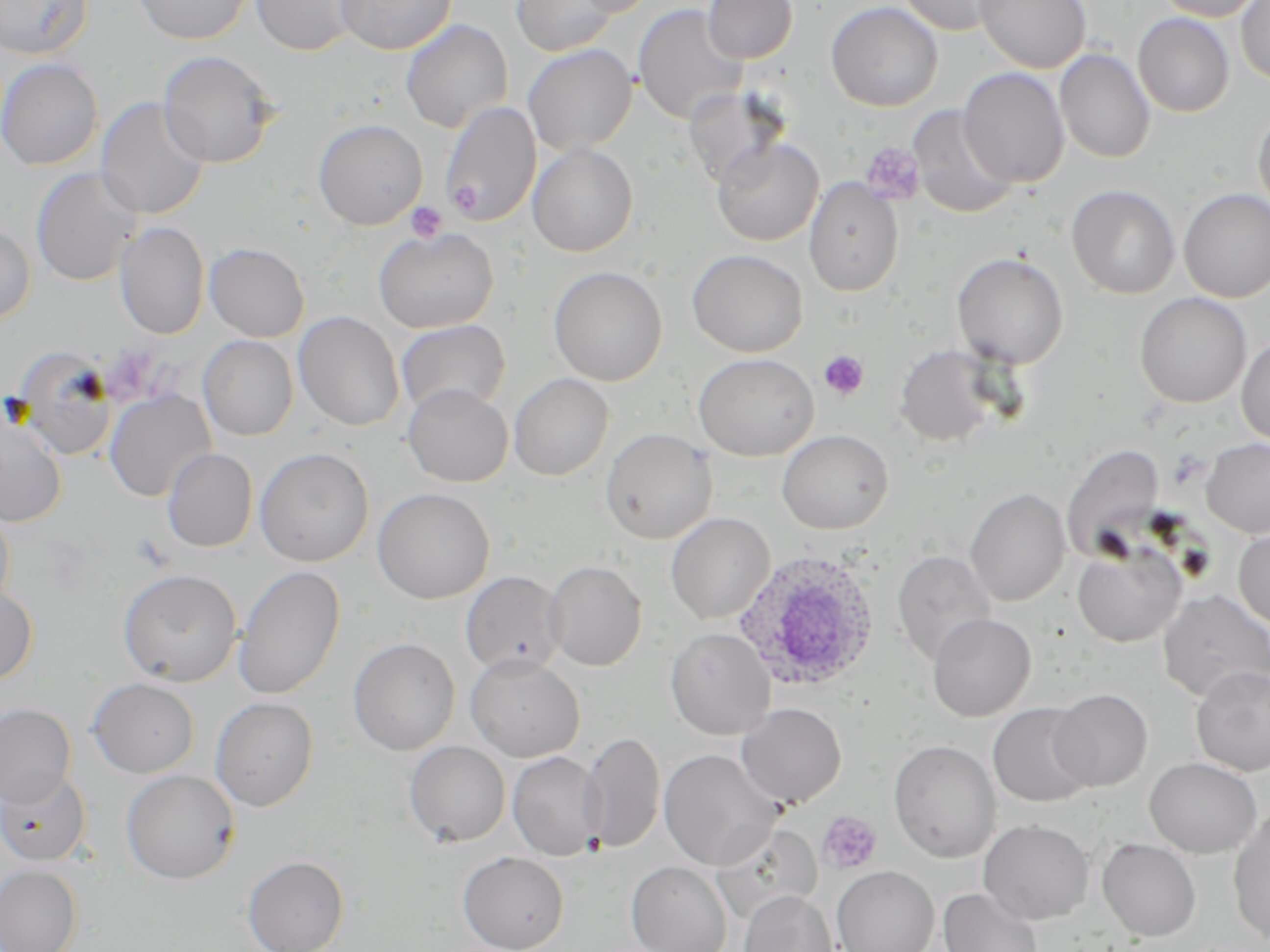
{
  "slide_level_diagnosis": "Plasmodium ovale",
  "preparation": "thin blood smear",
  "field_of_view": "single",
  "stain": "May-Grünwald-Giemsa",
  "magnification": "1000x",
  "platelet_locations": "approximate bounding boxes as named x1/y1/x2/y2 corners in pixels: (x1=859, y1=142, x2=926, y2=206), (x1=406, y1=202, x2=447, y2=243), (x1=818, y1=350, x2=869, y2=401), (x1=132, y1=534, x2=174, y2=570), (x1=816, y1=811, x2=882, y2=874)",
  "image_size": "1270×952 pixels",
  "modality": "optical microscopy",
  "uninfected_red_blood_cell_locations": "approximate bounding boxes as named x1/y1/x2/y2 corners in pixels: (x1=1, y1=0, x2=93, y2=59), (x1=133, y1=0, x2=254, y2=45), (x1=251, y1=0, x2=363, y2=56), (x1=337, y1=0, x2=456, y2=54), (x1=509, y1=0, x2=617, y2=56), (x1=574, y1=0, x2=659, y2=17), (x1=703, y1=0, x2=797, y2=64), (x1=897, y1=0, x2=1009, y2=36), (x1=975, y1=0, x2=1091, y2=73), (x1=1150, y1=0, x2=1267, y2=22), (x1=1236, y1=0, x2=1270, y2=85), (x1=826, y1=1, x2=943, y2=112), (x1=633, y1=4, x2=748, y2=125), (x1=1133, y1=13, x2=1235, y2=117), (x1=400, y1=19, x2=513, y2=133), (x1=523, y1=44, x2=637, y2=155), (x1=1054, y1=49, x2=1155, y2=163), (x1=158, y1=51, x2=278, y2=168), (x1=0, y1=58, x2=103, y2=171), (x1=958, y1=68, x2=1070, y2=188), (x1=683, y1=86, x2=789, y2=188), (x1=96, y1=97, x2=210, y2=220), (x1=440, y1=101, x2=541, y2=227), (x1=908, y1=105, x2=1020, y2=219), (x1=1253, y1=108, x2=1270, y2=218), (x1=313, y1=118, x2=427, y2=230), (x1=712, y1=136, x2=823, y2=246), (x1=527, y1=143, x2=638, y2=257), (x1=31, y1=167, x2=143, y2=286), (x1=804, y1=177, x2=904, y2=296), (x1=1066, y1=185, x2=1181, y2=299), (x1=1179, y1=189, x2=1270, y2=303), (x1=0, y1=222, x2=36, y2=325), (x1=114, y1=222, x2=210, y2=339), (x1=374, y1=227, x2=499, y2=333), (x1=205, y1=242, x2=309, y2=342), (x1=687, y1=249, x2=808, y2=357), (x1=951, y1=252, x2=1069, y2=369), (x1=548, y1=266, x2=668, y2=386), (x1=1135, y1=292, x2=1252, y2=408), (x1=293, y1=311, x2=404, y2=431), (x1=395, y1=319, x2=510, y2=417), (x1=198, y1=335, x2=298, y2=441), (x1=1236, y1=335, x2=1270, y2=445), (x1=895, y1=344, x2=1002, y2=447), (x1=693, y1=353, x2=819, y2=461), (x1=14, y1=369, x2=119, y2=464), (x1=509, y1=373, x2=613, y2=480), (x1=403, y1=384, x2=512, y2=487), (x1=104, y1=390, x2=216, y2=502), (x1=0, y1=412, x2=67, y2=528), (x1=600, y1=427, x2=717, y2=544), (x1=777, y1=429, x2=894, y2=534), (x1=1201, y1=438, x2=1270, y2=538), (x1=1061, y1=444, x2=1164, y2=562), (x1=161, y1=447, x2=258, y2=553), (x1=254, y1=447, x2=374, y2=566), (x1=373, y1=488, x2=494, y2=604), (x1=965, y1=488, x2=1071, y2=606), (x1=0, y1=506, x2=15, y2=614), (x1=666, y1=513, x2=775, y2=624), (x1=1233, y1=527, x2=1270, y2=632), (x1=1072, y1=541, x2=1187, y2=648), (x1=892, y1=549, x2=996, y2=665), (x1=543, y1=559, x2=647, y2=671), (x1=233, y1=566, x2=346, y2=700), (x1=118, y1=569, x2=243, y2=687), (x1=461, y1=570, x2=566, y2=675), (x1=0, y1=584, x2=38, y2=685), (x1=1157, y1=590, x2=1270, y2=704), (x1=928, y1=613, x2=1036, y2=721), (x1=665, y1=627, x2=775, y2=739), (x1=348, y1=637, x2=460, y2=755), (x1=465, y1=654, x2=585, y2=762), (x1=1191, y1=666, x2=1270, y2=776), (x1=88, y1=678, x2=199, y2=778), (x1=1049, y1=689, x2=1152, y2=791), (x1=211, y1=697, x2=319, y2=811), (x1=737, y1=703, x2=846, y2=808), (x1=988, y1=703, x2=1095, y2=808), (x1=0, y1=704, x2=76, y2=807), (x1=580, y1=732, x2=665, y2=853), (x1=889, y1=740, x2=1001, y2=862), (x1=405, y1=741, x2=510, y2=847), (x1=658, y1=749, x2=782, y2=870), (x1=507, y1=752, x2=605, y2=861), (x1=1145, y1=757, x2=1262, y2=858), (x1=0, y1=769, x2=91, y2=865), (x1=122, y1=769, x2=240, y2=883), (x1=1227, y1=809, x2=1270, y2=944), (x1=978, y1=819, x2=1093, y2=925), (x1=712, y1=823, x2=823, y2=923), (x1=1097, y1=838, x2=1201, y2=941), (x1=458, y1=851, x2=569, y2=952), (x1=243, y1=855, x2=349, y2=952), (x1=626, y1=861, x2=732, y2=952), (x1=0, y1=865, x2=83, y2=952), (x1=832, y1=866, x2=939, y2=952), (x1=938, y1=888, x2=1043, y2=952), (x1=740, y1=890, x2=837, y2=952)",
  "plasmodium_ovale_infected_red_blood_cell_locations": "approximate bounding boxes as named x1/y1/x2/y2 corners in pixels: (x1=732, y1=549, x2=883, y2=692)"
}